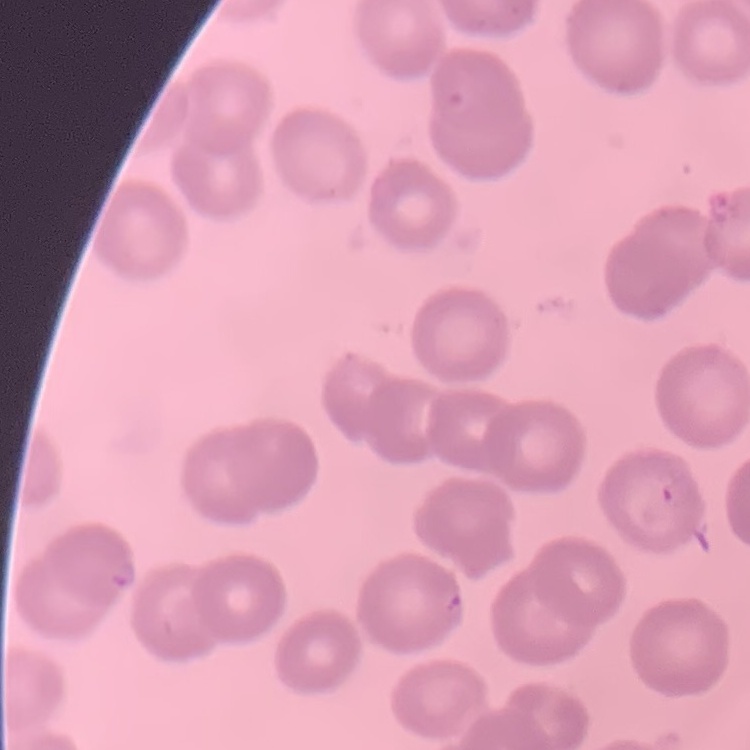
red blood cell morphology = no rouleaux formation
stain = Field's or Giemsa
preparation = thin peripheral smear
image type = square crop of a larger photomicrograph